Give the position of every Plasmodium parasite.
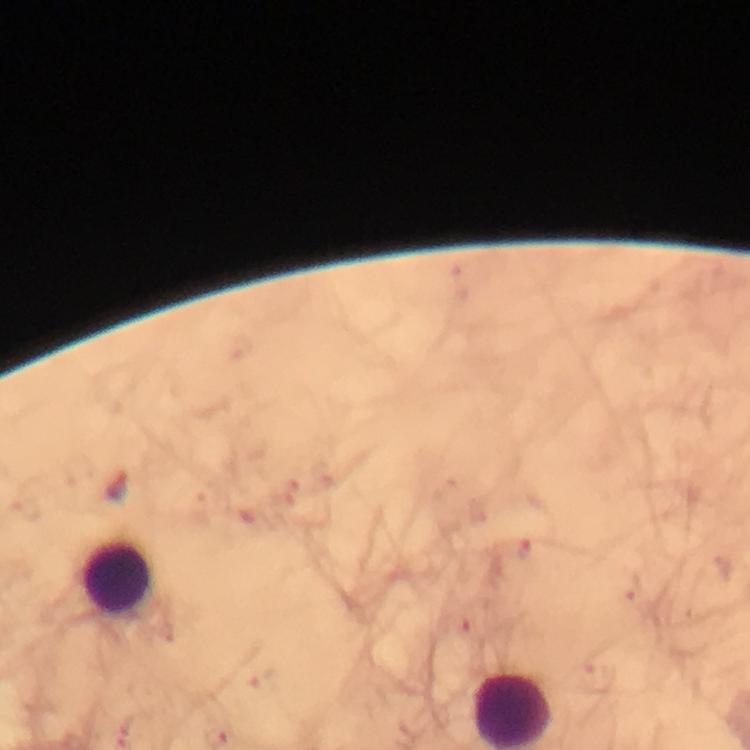
No Plasmodium parasites seen.

Approximate centers as (x, y) in pixels. Leukocyte locations: (117, 579). 100x magnification. A crop from one field of view. From a malaria diagnostic workup. Image is 750×750 pixels. Photographed with a smartphone mounted on the microscope. Giemsa stain. Immersion oil applied. Thick smear.